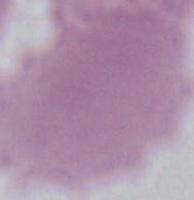
Photomicrograph. Captured at 1000x magnification. An erythrocyte is seen.